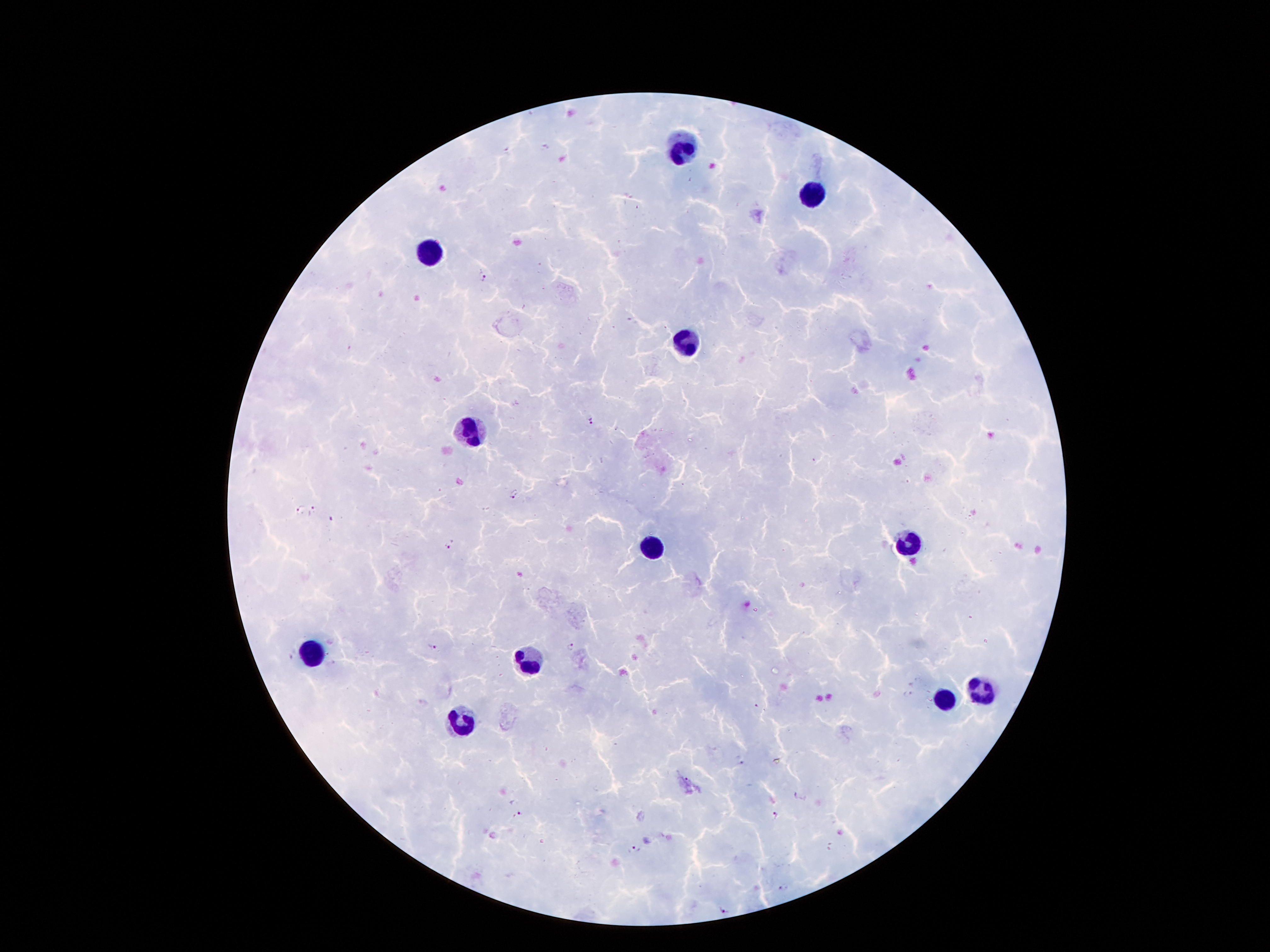

Approximate centers as {x, y} in pixels.
Summary:
  - Leukocyte locations: {682, 149}, {811, 195}, {428, 252}, {687, 344}, {471, 429}, {905, 544}, {652, 545}, {309, 647}, {532, 661}, {981, 690}, {943, 699}, {462, 720}
  - Malaria parasite locations: {482, 278}, {590, 420}, {514, 493}, {299, 510}, {314, 510}, {450, 545}, {433, 646}, {570, 647}, {908, 692}, {757, 705}, {519, 812}, {775, 816}, {634, 850}, {724, 911}
  - Stain: Giemsa
  - Preparation: thick peripheral-blood smear
  - Image size: 1270×952 pixels
  - Magnification: 100x
  - Patient malaria status: positive for Plasmodium falciparum
  - Capture: smartphone through the microscope eyepiece
  - Field of view: one from this slide